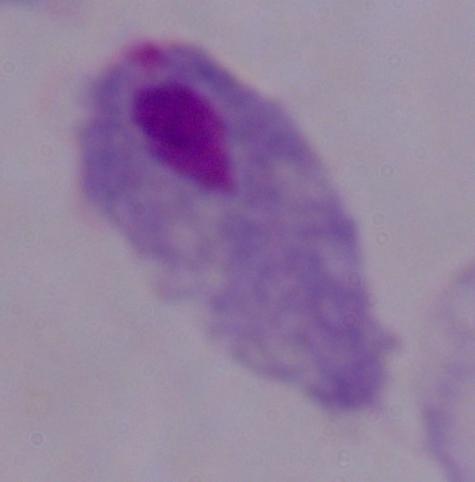

modality: micrograph
identification: trichomonad
magnification: 1000x